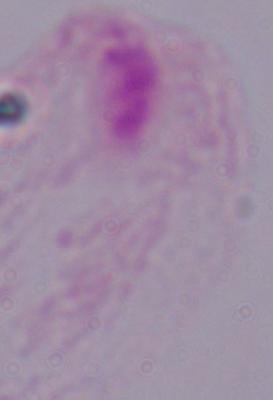
{
  "modality": "photomicrograph",
  "identification": "trichomonad",
  "magnification": "1000x"
}